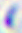

{
  "magnification": "400x",
  "modality": "photomicrograph",
  "identification": "Toxoplasma gondii"
}